Classify this cell by malaria status.
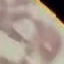
It is uninfected.

Automatically extracted cell patch, resized to 64 × 64 pixels. Giemsa stain. Acquired by smartphone through the microscope eyepiece. Thin blood smear.